Name the parasite shown.
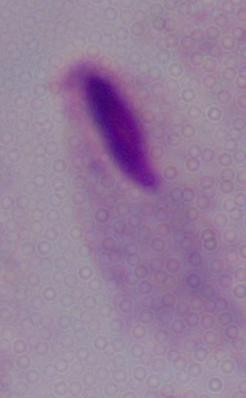
A trichomonad.

modality = photomicrograph
magnification = 1000x